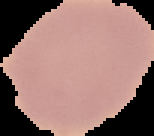
Summary:
  - Image type: cell region segmented out of the field of view; surrounding area masked to black
  - Preparation: thin blood film
  - Result: no malaria parasites detected
  - Image size: 154×136 pixels